Describe the morphology of the red blood cells.
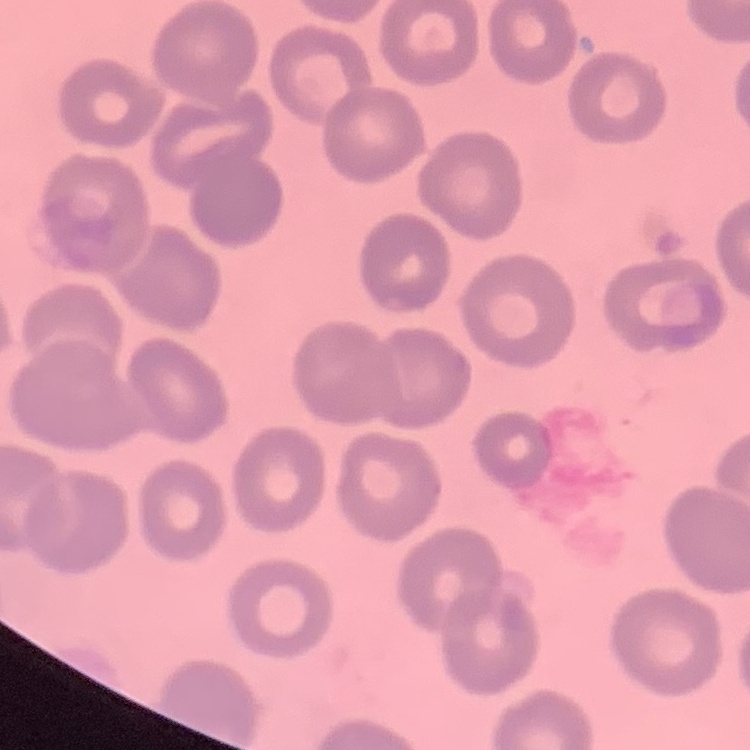

They show no rouleaux formation.

Summary:
  - Image type: one tile cut from a larger photomicrograph
  - Stain: Field's or Giemsa
  - Preparation: thin blood film